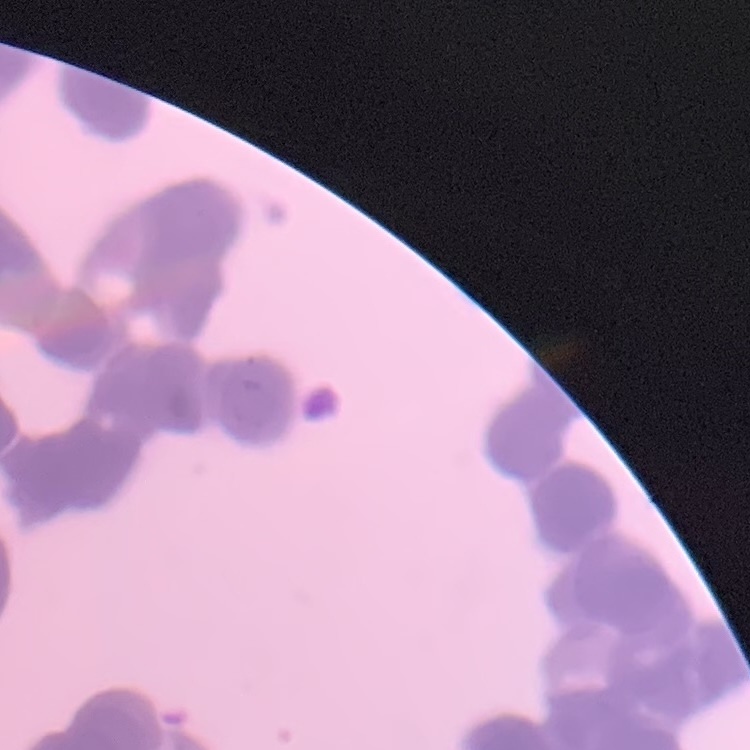

erythrocyte morphology = rouleaux formation
preparation = thin peripheral smear
stain = Field's or Giemsa
image type = square crop of a larger photomicrograph